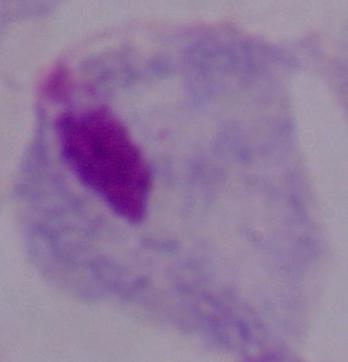 1000x magnification. Micrograph. A trichomonad is shown.